Report the malaria status of this cell.
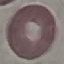

Uninfected.

Acquired by smartphone through the microscope eyepiece. Thin blood smear. Giemsa stain. Cell patch, automatically extracted from a larger field of view and resized to 64 × 64 pixels.